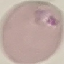
Summary:
  - Result: malaria parasites identified
  - Preparation: thin blood smear
  - Image type: automatically extracted cell patch, resized to 64 × 64 pixels
  - Capture: smartphone camera at the microscope eyepiece
  - Stain: Giemsa